Assess for malaria.
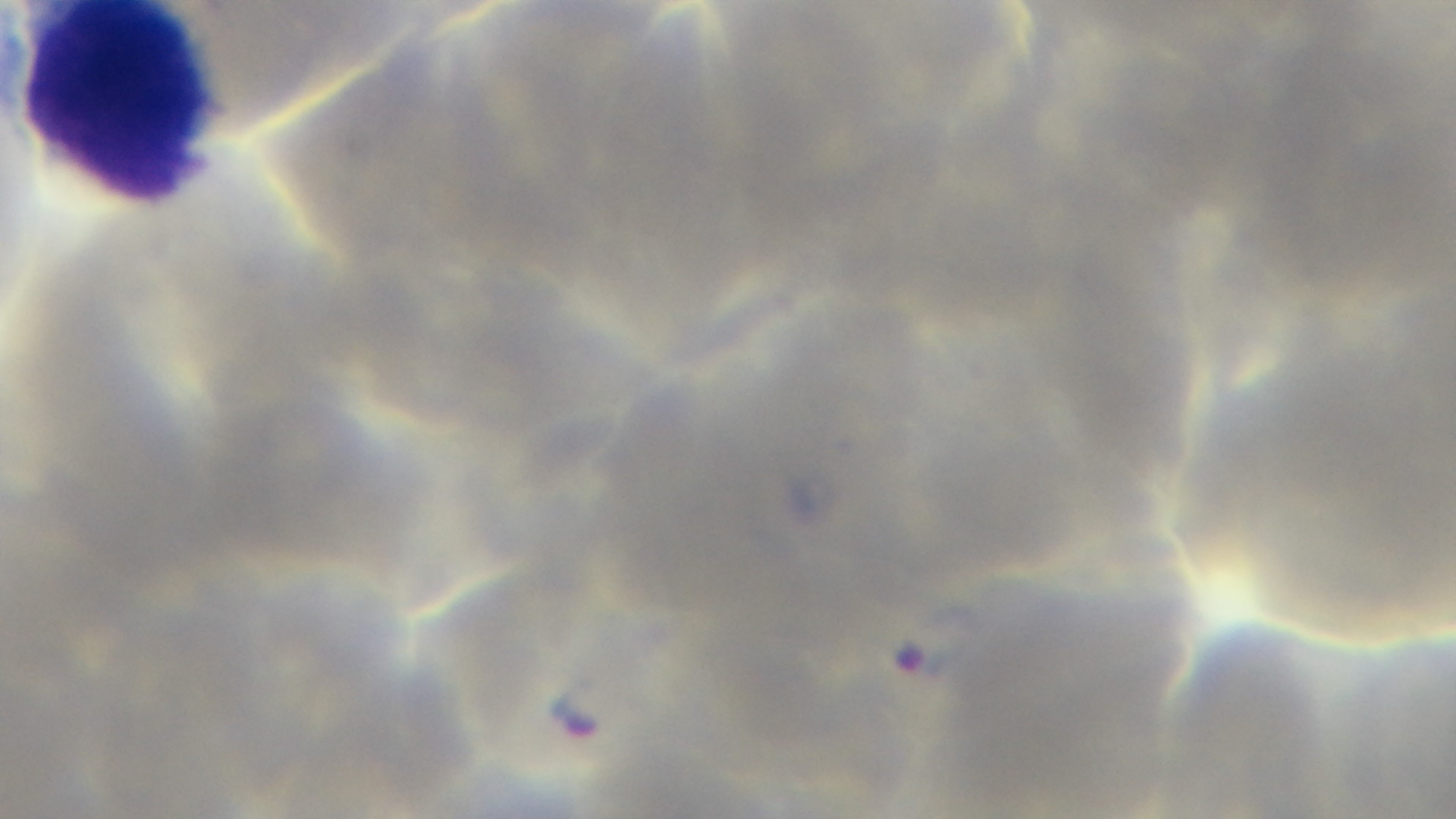

It is infected.

{
  "objective": "100x oil immersion",
  "preparation": "thin",
  "field_of_view": "one from the slide",
  "modality": "light microscopy",
  "capture": "mounted 4K digital camera",
  "stain": "Giemsa"
}